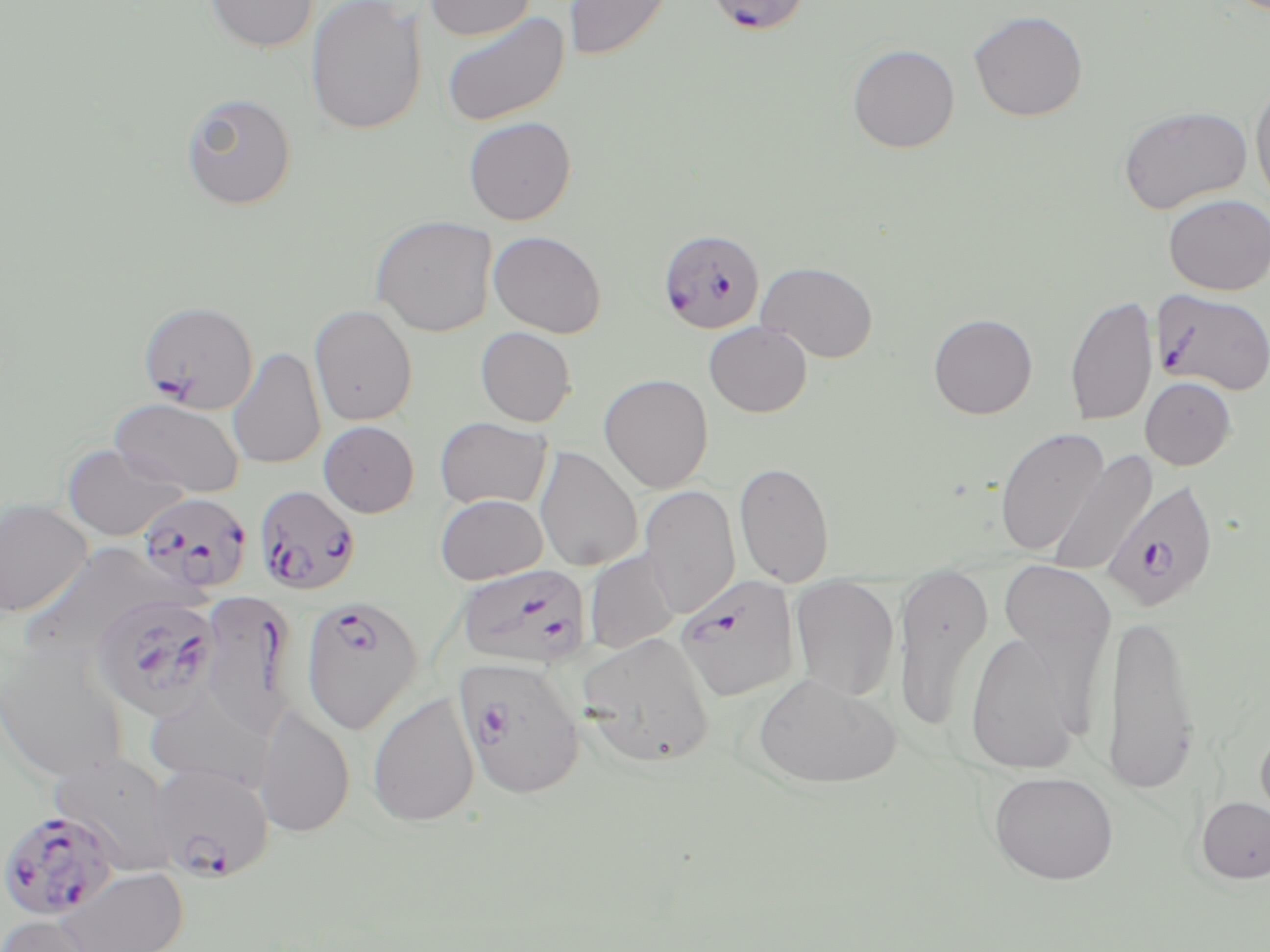
slide-level diagnosis = Plasmodium falciparum
preparation = thin blood smear
Plasmodium falciparum-infected red blood cell locations (subset) = approximate bounding boxes as named x1/y1/x2/y2 corners in pixels: (x1=714, y1=0, x2=808, y2=37), (x1=657, y1=229, x2=766, y2=334), (x1=1153, y1=288, x2=1270, y2=395), (x1=138, y1=300, x2=259, y2=414), (x1=1102, y1=479, x2=1219, y2=614), (x1=253, y1=484, x2=361, y2=595), (x1=137, y1=492, x2=252, y2=595), (x1=457, y1=562, x2=591, y2=669), (x1=91, y1=593, x2=221, y2=722), (x1=198, y1=593, x2=296, y2=740), (x1=300, y1=596, x2=423, y2=733), (x1=455, y1=655, x2=585, y2=799), (x1=148, y1=762, x2=275, y2=883), (x1=0, y1=808, x2=120, y2=923)
field of view = one of a larger specimen
magnification = 1000x
stain = May-Grünwald-Giemsa
modality = optical microscopy
image size = 1270×952 pixels
uninfected red blood cell locations (subset) = approximate bounding boxes as named x1/y1/x2/y2 corners in pixels: (x1=204, y1=0, x2=318, y2=53), (x1=306, y1=0, x2=427, y2=136), (x1=424, y1=0, x2=536, y2=41), (x1=563, y1=0, x2=675, y2=62), (x1=440, y1=9, x2=570, y2=128), (x1=967, y1=10, x2=1088, y2=122), (x1=847, y1=43, x2=960, y2=153), (x1=1250, y1=78, x2=1270, y2=210), (x1=180, y1=91, x2=297, y2=211), (x1=1117, y1=105, x2=1253, y2=214), (x1=462, y1=116, x2=577, y2=225), (x1=1163, y1=193, x2=1270, y2=295), (x1=370, y1=215, x2=497, y2=336), (x1=488, y1=230, x2=607, y2=338), (x1=757, y1=261, x2=879, y2=363), (x1=1064, y1=292, x2=1158, y2=427), (x1=309, y1=304, x2=418, y2=426), (x1=929, y1=313, x2=1037, y2=419), (x1=704, y1=321, x2=812, y2=418), (x1=475, y1=326, x2=577, y2=427), (x1=227, y1=347, x2=326, y2=469), (x1=599, y1=374, x2=713, y2=493), (x1=1140, y1=376, x2=1236, y2=470), (x1=109, y1=397, x2=245, y2=497), (x1=435, y1=417, x2=552, y2=510), (x1=318, y1=420, x2=419, y2=517), (x1=995, y1=427, x2=1109, y2=556), (x1=63, y1=443, x2=186, y2=540), (x1=534, y1=445, x2=643, y2=572), (x1=1047, y1=448, x2=1158, y2=577), (x1=734, y1=461, x2=835, y2=587), (x1=639, y1=485, x2=741, y2=620), (x1=435, y1=494, x2=548, y2=584), (x1=0, y1=498, x2=93, y2=617), (x1=20, y1=544, x2=182, y2=659), (x1=586, y1=550, x2=680, y2=654), (x1=997, y1=558, x2=1116, y2=699), (x1=893, y1=566, x2=993, y2=732), (x1=789, y1=577, x2=899, y2=701), (x1=1104, y1=608, x2=1201, y2=794), (x1=963, y1=628, x2=1083, y2=776), (x1=576, y1=631, x2=716, y2=768), (x1=0, y1=640, x2=130, y2=783), (x1=752, y1=672, x2=901, y2=788), (x1=143, y1=683, x2=276, y2=791), (x1=367, y1=692, x2=479, y2=827), (x1=255, y1=704, x2=355, y2=838), (x1=1254, y1=720, x2=1270, y2=841), (x1=51, y1=752, x2=181, y2=875), (x1=987, y1=771, x2=1119, y2=885), (x1=1196, y1=796, x2=1270, y2=884), (x1=54, y1=867, x2=191, y2=952), (x1=1, y1=915, x2=108, y2=952)